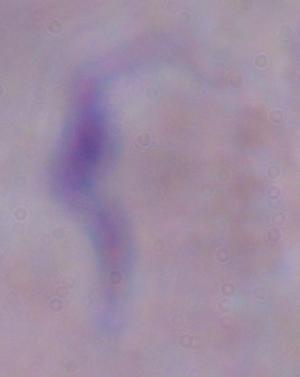
Photomicrograph. A trypanosome is seen. 1000x magnification.